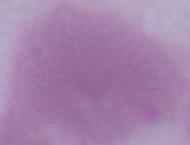

Summary:
  - Identification: red blood cell
  - Magnification: 1000x
  - Modality: micrograph